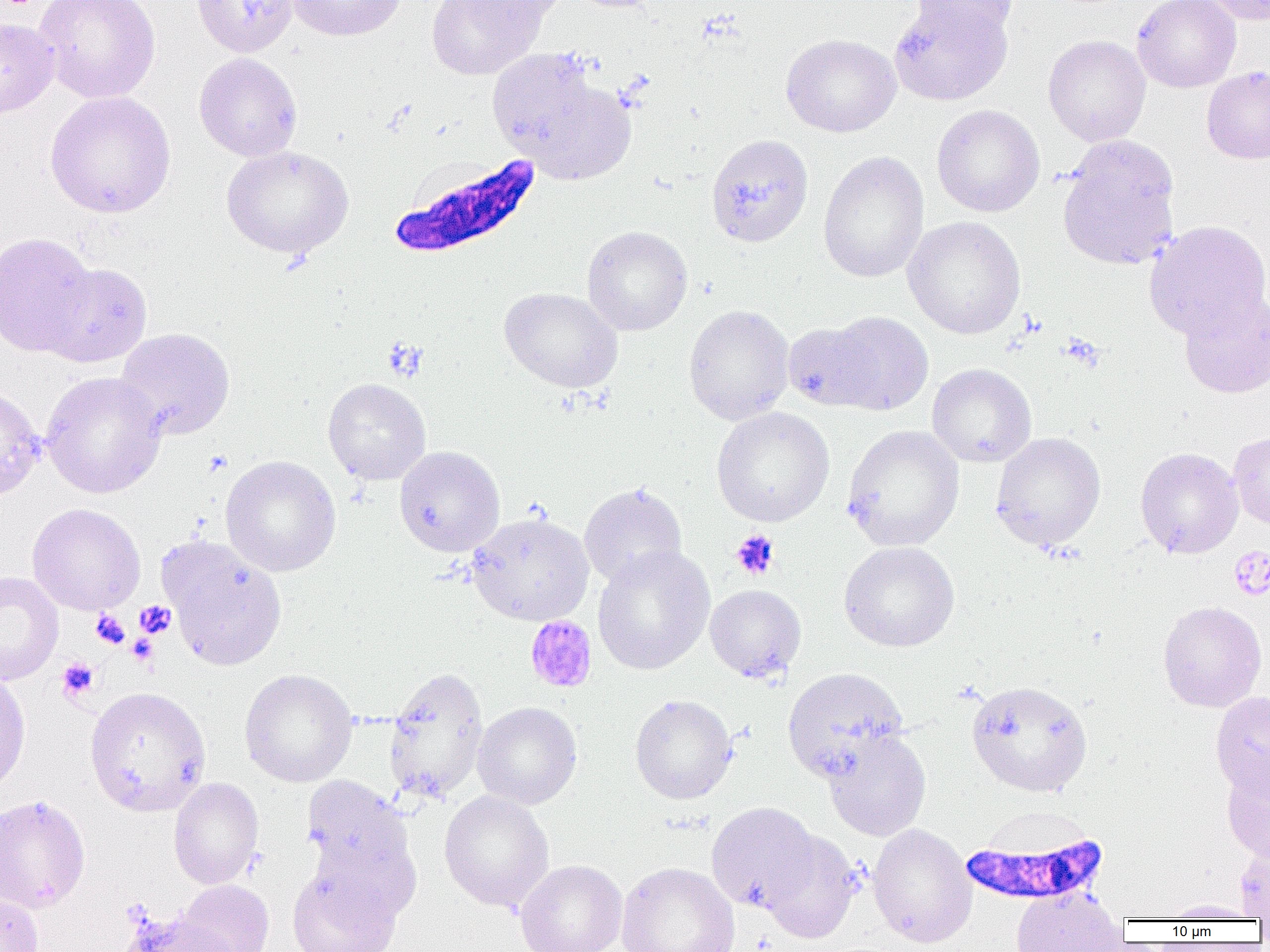 Approximate bounding boxes as (x1,y1)-(x2,y2) corner pairs in pixels. Uninfected red blood cell locations: (35,0)-(161,104), (192,0)-(299,56), (286,0)-(406,41), (427,0)-(546,80), (454,0)-(570,24), (563,0)-(662,13), (889,0)-(1012,106), (910,0)-(1016,41), (1132,0)-(1241,92), (1198,0)-(1270,25), (0,18)-(59,119), (780,33)-(901,138), (1043,34)-(1151,146), (486,49)-(606,163), (194,53)-(303,162), (1201,66)-(1270,164), (523,77)-(637,185), (44,91)-(176,219), (931,104)-(1045,217), (705,133)-(814,248), (1056,135)-(1181,271), (221,145)-(353,260), (818,151)-(929,284), (903,216)-(1026,340), (1144,220)-(1270,340), (582,225)-(693,336), (0,232)-(98,357), (39,262)-(153,368), (499,287)-(623,393), (1178,290)-(1270,399), (683,304)-(794,426), (824,311)-(933,415), (783,321)-(882,411), (114,327)-(235,440), (927,363)-(1036,467), (40,371)-(167,498), (322,377)-(431,485), (0,383)-(45,502), (711,406)-(835,527), (842,424)-(964,551), (1228,431)-(1270,530), (991,432)-(1106,551), (394,445)-(505,557), (1135,447)-(1243,559), (220,455)-(342,577), (579,483)-(687,588), (27,503)-(146,615), (466,512)-(594,626), (158,536)-(288,670), (838,540)-(960,652), (592,545)-(715,675), (0,571)-(64,685), (705,584)-(806,682), (1157,601)-(1267,712), (383,666)-(489,803), (782,667)-(908,783), (0,668)-(31,798), (239,668)-(358,787), (967,680)-(1093,797), (84,686)-(211,816), (1210,692)-(1270,798), (629,693)-(738,804), (472,701)-(582,809), (824,730)-(931,841), (1222,763)-(1270,863), (301,776)-(411,882), (168,777)-(264,889), (439,791)-(554,912), (0,794)-(91,913), (707,802)-(821,911), (867,823)-(976,948), (759,830)-(862,943), (1235,843)-(1270,922), (515,859)-(627,952), (286,861)-(402,952), (616,861)-(741,952), (175,880)-(274,952), (1011,887)-(1127,952), (0,891)-(44,952), (1159,899)-(1261,921), (121,910)-(241,951). Plasmodium falciparum-infected red blood cell locations: (391,154)-(543,260), (958,828)-(1110,907). Platelet locations: (1061,334)-(1104,371), (202,450)-(232,477), (729,530)-(780,580), (1228,546)-(1270,600), (135,600)-(176,639), (91,610)-(130,648), (524,616)-(597,693), (127,633)-(158,664), (57,658)-(99,701). Slide-level diagnosis: Plasmodium falciparum. Single field of view. Image is 1270×952 pixels. Light microscopy. Thin blood smear. 1000x magnification.